Outline each uninfected red blood cell.
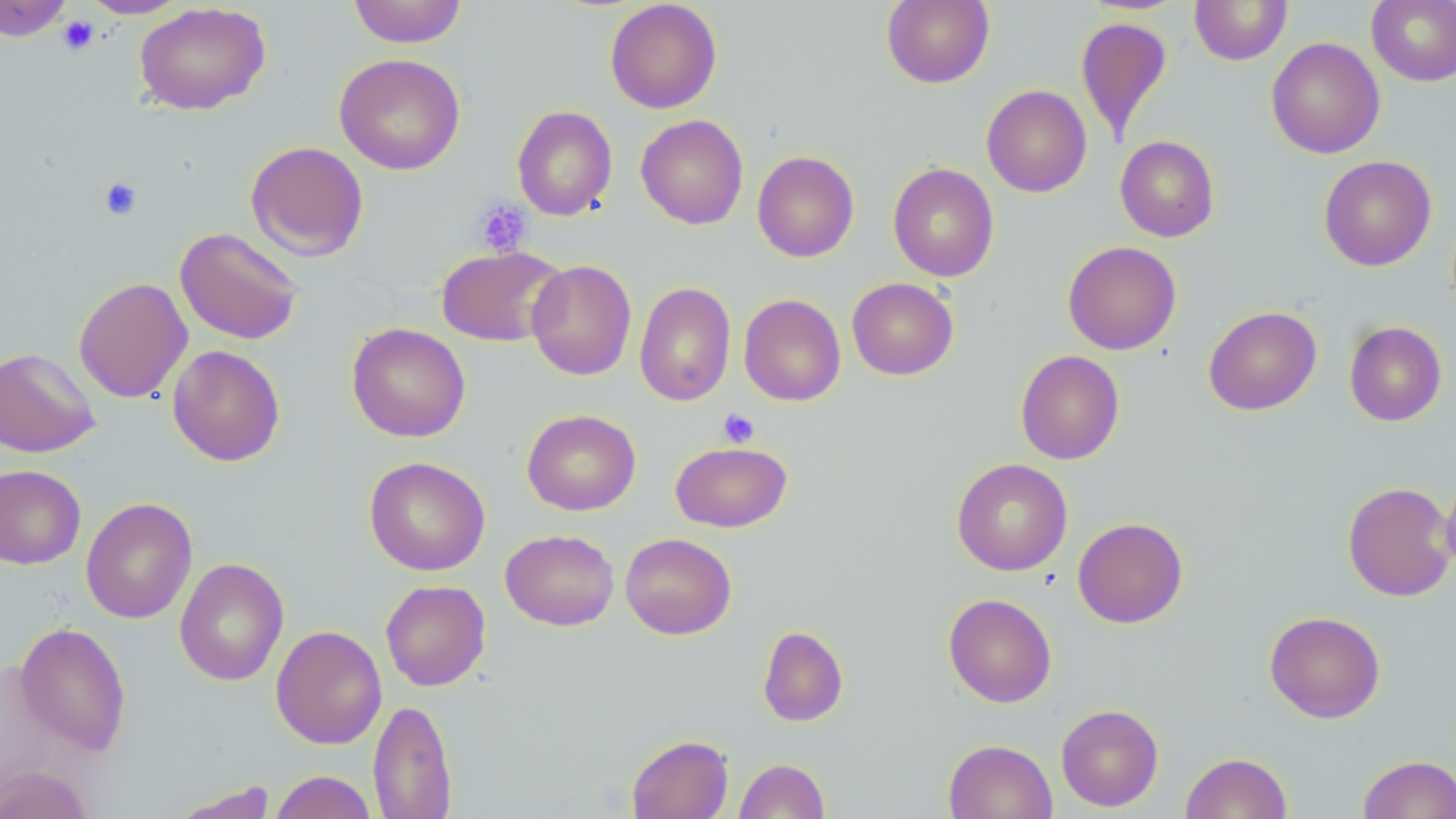
Approximate bounding boxes as (x1, y1, x2, y2) in pixels.
Uninfected red blood cells: (0, 0, 73, 41), (80, 0, 189, 18), (348, 0, 467, 48), (605, 0, 722, 114), (881, 0, 995, 88), (1189, 0, 1292, 65), (1366, 0, 1456, 87), (134, 2, 271, 116), (1075, 16, 1173, 144), (1265, 37, 1385, 159), (334, 53, 465, 175), (981, 85, 1092, 197), (512, 105, 618, 221), (635, 114, 748, 230), (1115, 135, 1220, 241), (245, 141, 369, 261), (752, 150, 859, 262), (1318, 155, 1437, 271), (887, 162, 999, 281), (174, 226, 305, 345), (1062, 241, 1181, 355), (435, 244, 567, 347), (526, 259, 637, 381), (73, 277, 193, 403), (847, 277, 959, 380), (634, 281, 735, 407), (739, 294, 846, 406), (1203, 305, 1322, 415), (1344, 321, 1447, 426), (347, 323, 471, 443), (167, 344, 285, 466), (0, 348, 101, 458), (1015, 350, 1125, 464), (522, 409, 641, 515), (671, 441, 792, 532), (364, 456, 490, 576), (951, 458, 1073, 576), (0, 464, 85, 569), (1441, 468, 1456, 578), (1342, 481, 1455, 601), (80, 497, 197, 624), (1073, 517, 1188, 628), (500, 529, 619, 631), (620, 532, 737, 640), (174, 557, 289, 686), (380, 579, 491, 691), (943, 593, 1057, 708), (1264, 610, 1386, 723), (15, 621, 132, 756), (271, 625, 387, 749), (757, 625, 848, 727), (368, 698, 457, 819), (1055, 704, 1164, 812), (626, 734, 733, 819), (943, 739, 1057, 819), (1180, 752, 1292, 819), (1358, 754, 1456, 818), (734, 758, 830, 819), (0, 765, 94, 819), (270, 770, 377, 819), (169, 781, 278, 818).

Summary:
  - Platelet locations: (57, 15, 99, 55), (98, 177, 143, 222), (472, 197, 532, 257), (717, 408, 759, 448)
  - Slide-level diagnosis: no evidence of blood parasites
  - Field of view: one of a larger specimen
  - Magnification: 1000x
  - Stain: May-Grünwald-Giemsa
  - Modality: optical microscopy
  - Preparation: thin blood smear
  - Image size: 1456×819 pixels